State the blood parasite species.
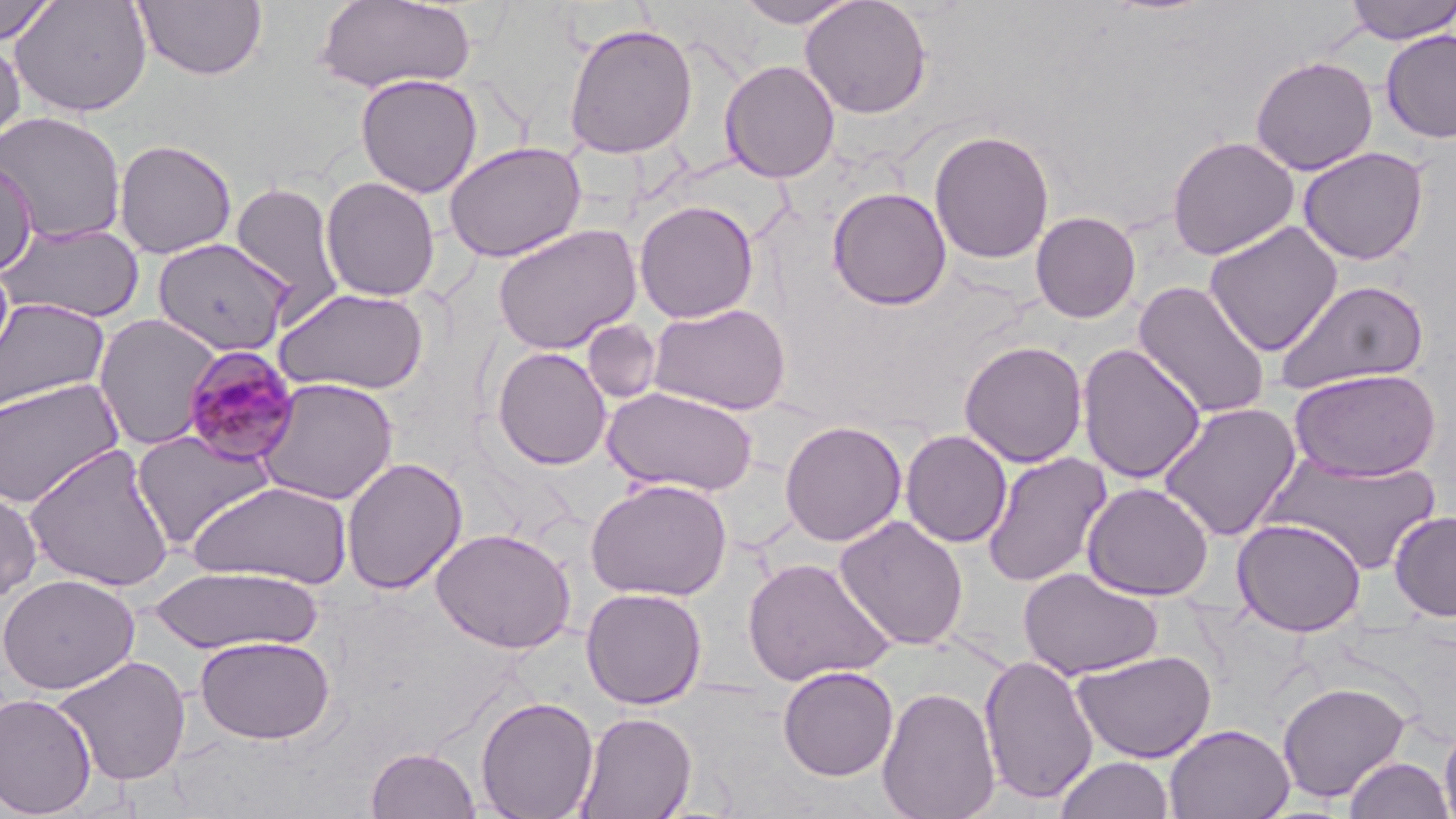

Plasmodium malariae.

Summary:
  - Coordinate format: approximate bounding boxes as named x1/y1/x2/y2 corners in pixels
  - Uninfected red blood cell locations: (x1=1, y1=0, x2=57, y2=45), (x1=11, y1=0, x2=152, y2=117), (x1=133, y1=0, x2=268, y2=81), (x1=732, y1=0, x2=863, y2=28), (x1=800, y1=0, x2=932, y2=119), (x1=1343, y1=0, x2=1456, y2=44), (x1=314, y1=1, x2=476, y2=94), (x1=562, y1=21, x2=699, y2=159), (x1=1380, y1=30, x2=1456, y2=144), (x1=0, y1=33, x2=26, y2=153), (x1=1250, y1=55, x2=1378, y2=176), (x1=718, y1=59, x2=840, y2=183), (x1=354, y1=73, x2=484, y2=198), (x1=1, y1=111, x2=127, y2=245), (x1=928, y1=129, x2=1055, y2=264), (x1=1166, y1=135, x2=1300, y2=260), (x1=113, y1=138, x2=238, y2=259), (x1=443, y1=141, x2=587, y2=263), (x1=1298, y1=146, x2=1429, y2=265), (x1=0, y1=155, x2=38, y2=277), (x1=320, y1=176, x2=441, y2=302), (x1=228, y1=181, x2=346, y2=322), (x1=826, y1=186, x2=952, y2=310), (x1=634, y1=200, x2=759, y2=323), (x1=1030, y1=211, x2=1142, y2=323), (x1=1203, y1=221, x2=1344, y2=356), (x1=0, y1=222, x2=145, y2=324), (x1=492, y1=223, x2=642, y2=355), (x1=151, y1=237, x2=293, y2=357), (x1=1272, y1=278, x2=1430, y2=395), (x1=1133, y1=280, x2=1273, y2=420), (x1=274, y1=286, x2=431, y2=396), (x1=0, y1=297, x2=110, y2=413), (x1=648, y1=302, x2=792, y2=415), (x1=92, y1=313, x2=223, y2=450), (x1=581, y1=320, x2=662, y2=405), (x1=959, y1=340, x2=1089, y2=468), (x1=1076, y1=343, x2=1207, y2=484), (x1=491, y1=346, x2=612, y2=470), (x1=1288, y1=367, x2=1441, y2=482), (x1=0, y1=377, x2=125, y2=508), (x1=254, y1=377, x2=400, y2=505), (x1=602, y1=386, x2=759, y2=497), (x1=1157, y1=402, x2=1302, y2=541), (x1=779, y1=420, x2=907, y2=546), (x1=900, y1=429, x2=1013, y2=548), (x1=132, y1=430, x2=277, y2=551), (x1=23, y1=443, x2=177, y2=592), (x1=982, y1=452, x2=1112, y2=588), (x1=1260, y1=453, x2=1443, y2=574), (x1=341, y1=457, x2=468, y2=594), (x1=585, y1=478, x2=733, y2=601), (x1=187, y1=480, x2=353, y2=589), (x1=1081, y1=481, x2=1215, y2=601), (x1=0, y1=483, x2=43, y2=605), (x1=1389, y1=509, x2=1456, y2=622), (x1=834, y1=515, x2=969, y2=651), (x1=1231, y1=517, x2=1367, y2=636), (x1=431, y1=528, x2=577, y2=654), (x1=743, y1=556, x2=894, y2=686), (x1=148, y1=564, x2=325, y2=655), (x1=1018, y1=567, x2=1163, y2=681), (x1=0, y1=573, x2=140, y2=695), (x1=580, y1=587, x2=708, y2=709), (x1=194, y1=635, x2=336, y2=745), (x1=1070, y1=649, x2=1217, y2=763), (x1=53, y1=654, x2=192, y2=786), (x1=978, y1=654, x2=1099, y2=805), (x1=778, y1=665, x2=899, y2=781), (x1=1276, y1=680, x2=1411, y2=803), (x1=877, y1=685, x2=1001, y2=819), (x1=0, y1=693, x2=98, y2=818), (x1=476, y1=695, x2=599, y2=819), (x1=574, y1=711, x2=697, y2=819), (x1=1439, y1=721, x2=1456, y2=819), (x1=1164, y1=723, x2=1294, y2=819), (x1=365, y1=746, x2=481, y2=819), (x1=1054, y1=756, x2=1174, y2=818), (x1=1342, y1=756, x2=1454, y2=819)
  - Plasmodium malariae-infected red blood cell locations: (x1=181, y1=345, x2=301, y2=466)
  - Preparation: thin blood film
  - Modality: optical microscopy
  - Field of view: one of a larger specimen
  - Image size: 1456×819 pixels
  - Stain: May-Grünwald-Giemsa
  - Magnification: 1000x